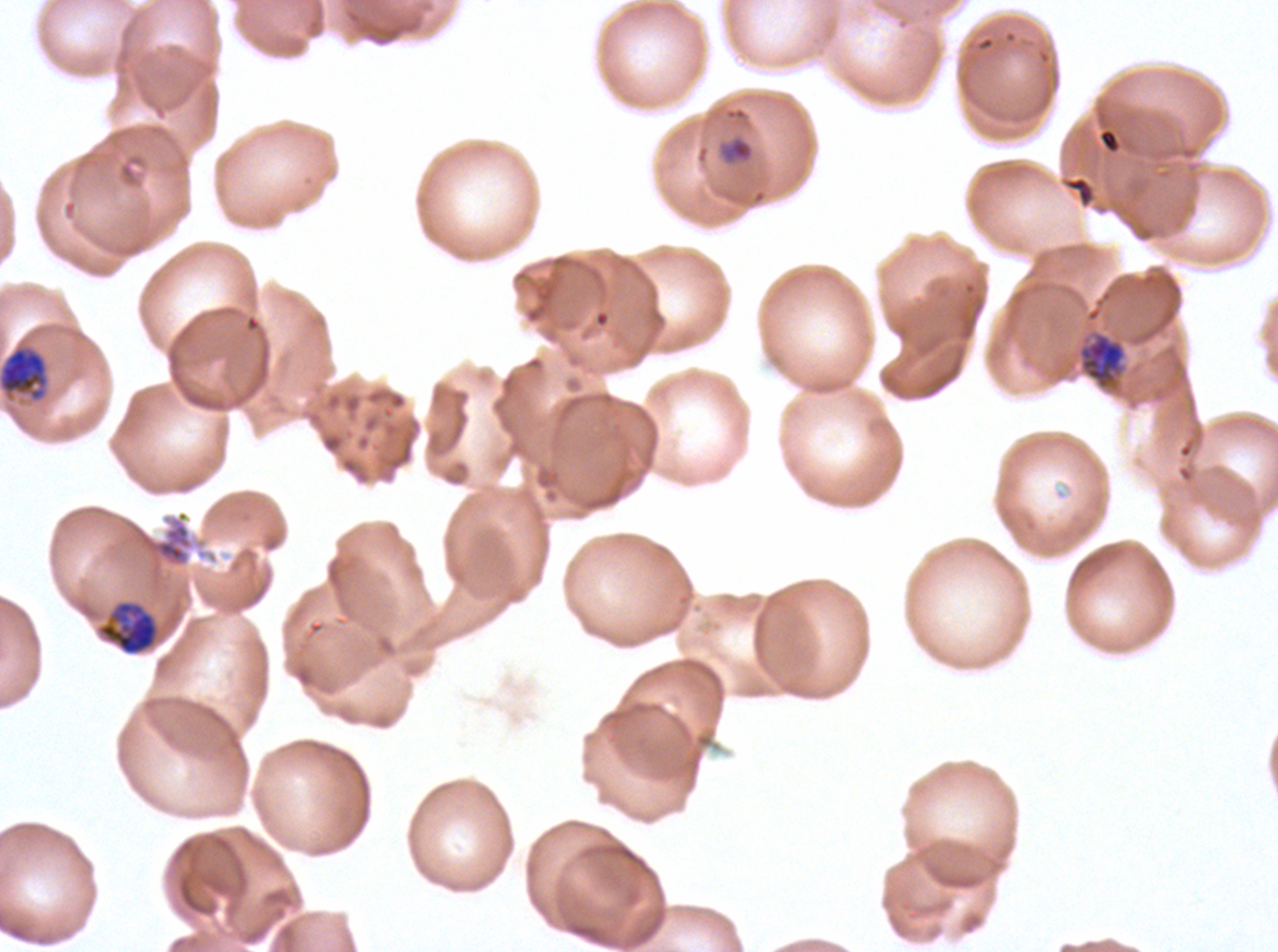

notation = approximate bounding boxes as [x1, y1, x2, y2] in pixels
late-ring/early-trophozoite locations = [721, 137, 754, 163]
debris locations = [136, 510, 193, 567]
late trophozoite locations = [1077, 330, 1127, 390], [0, 345, 49, 402], [98, 601, 159, 656]
specimen = ex-vivo Plasmodium falciparum culture from a patient in The Gambia, grown for 24 to 48 hours
stain = Giemsa
life-cycle stages observed = late-ring/early-trophozoite, late trophozoite
field of view = one sub-image of a larger composite
image size = 1278×952 pixels
preparation = thin blood film